Outline each Plasmodium falciparum-infected red blood cell.
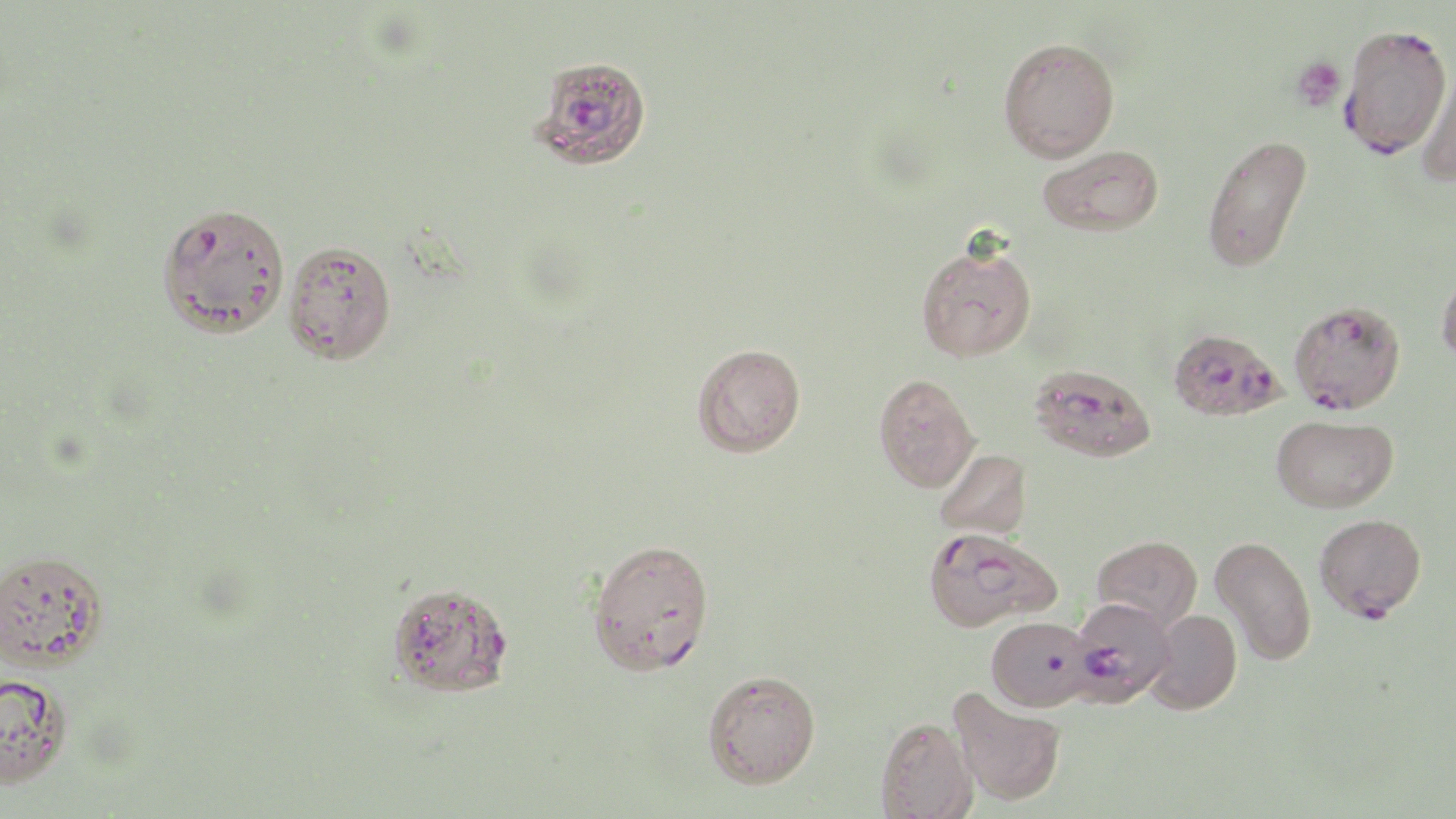

Approximate bounding boxes as named x1/y1/x2/y2 corners in pixels.
Plasmodium falciparum-infected red blood cells: (x1=1338, y1=22, x2=1451, y2=158), (x1=531, y1=55, x2=652, y2=170), (x1=1289, y1=300, x2=1406, y2=414), (x1=1170, y1=333, x2=1291, y2=428), (x1=1028, y1=363, x2=1157, y2=463), (x1=1314, y1=513, x2=1427, y2=621), (x1=922, y1=526, x2=1060, y2=632), (x1=587, y1=538, x2=715, y2=675), (x1=386, y1=582, x2=514, y2=699), (x1=1068, y1=595, x2=1182, y2=717), (x1=985, y1=616, x2=1095, y2=712).

Summary:
  - Uninfected red blood cell locations: (x1=998, y1=37, x2=1120, y2=162), (x1=1416, y1=63, x2=1456, y2=188), (x1=1202, y1=133, x2=1312, y2=272), (x1=1038, y1=144, x2=1164, y2=236), (x1=156, y1=202, x2=291, y2=338), (x1=282, y1=240, x2=397, y2=364), (x1=915, y1=242, x2=1037, y2=362), (x1=1436, y1=263, x2=1456, y2=366), (x1=692, y1=343, x2=806, y2=457), (x1=873, y1=373, x2=980, y2=492), (x1=1273, y1=415, x2=1400, y2=514), (x1=934, y1=448, x2=1031, y2=540), (x1=1092, y1=535, x2=1202, y2=632), (x1=1209, y1=535, x2=1316, y2=665), (x1=0, y1=548, x2=109, y2=671), (x1=1147, y1=608, x2=1242, y2=714), (x1=702, y1=670, x2=821, y2=788), (x1=0, y1=672, x2=73, y2=789), (x1=948, y1=687, x2=1067, y2=807), (x1=876, y1=716, x2=978, y2=819)
  - Platelet locations: (x1=1291, y1=56, x2=1346, y2=111)
  - Slide-level diagnosis: Plasmodium falciparum
  - Stain: May-Grünwald-Giemsa
  - Field of view: single
  - Modality: optical microscopy
  - Preparation: thin blood smear
  - Magnification: 1000x
  - Image size: 1456×819 pixels